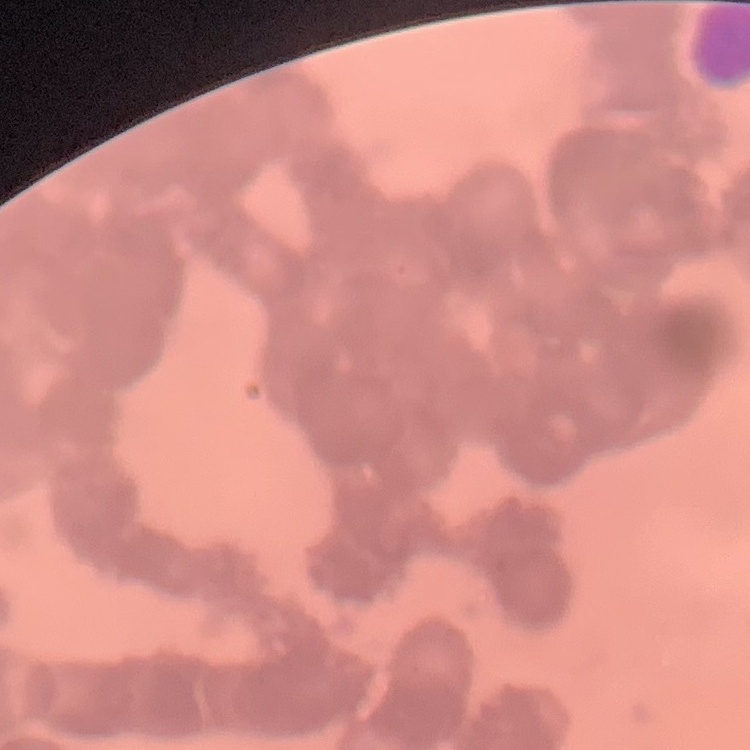

red blood cell morphology = rouleaux formation
preparation = thin blood smear
stain = Field's or Giemsa
image type = square crop of a larger photomicrograph